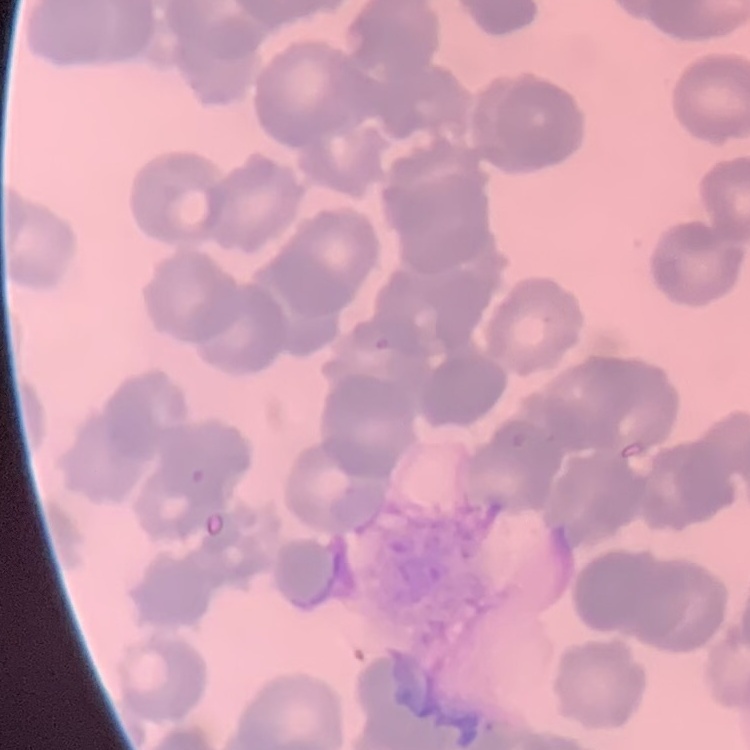
{
  "red_blood_cell_morphology": "rouleaux formation",
  "image_type": "square crop of a larger photomicrograph",
  "stain": "Field's or Giemsa",
  "preparation": "thin blood film"
}